Give the position of every malaria parasite and every leukocyte.
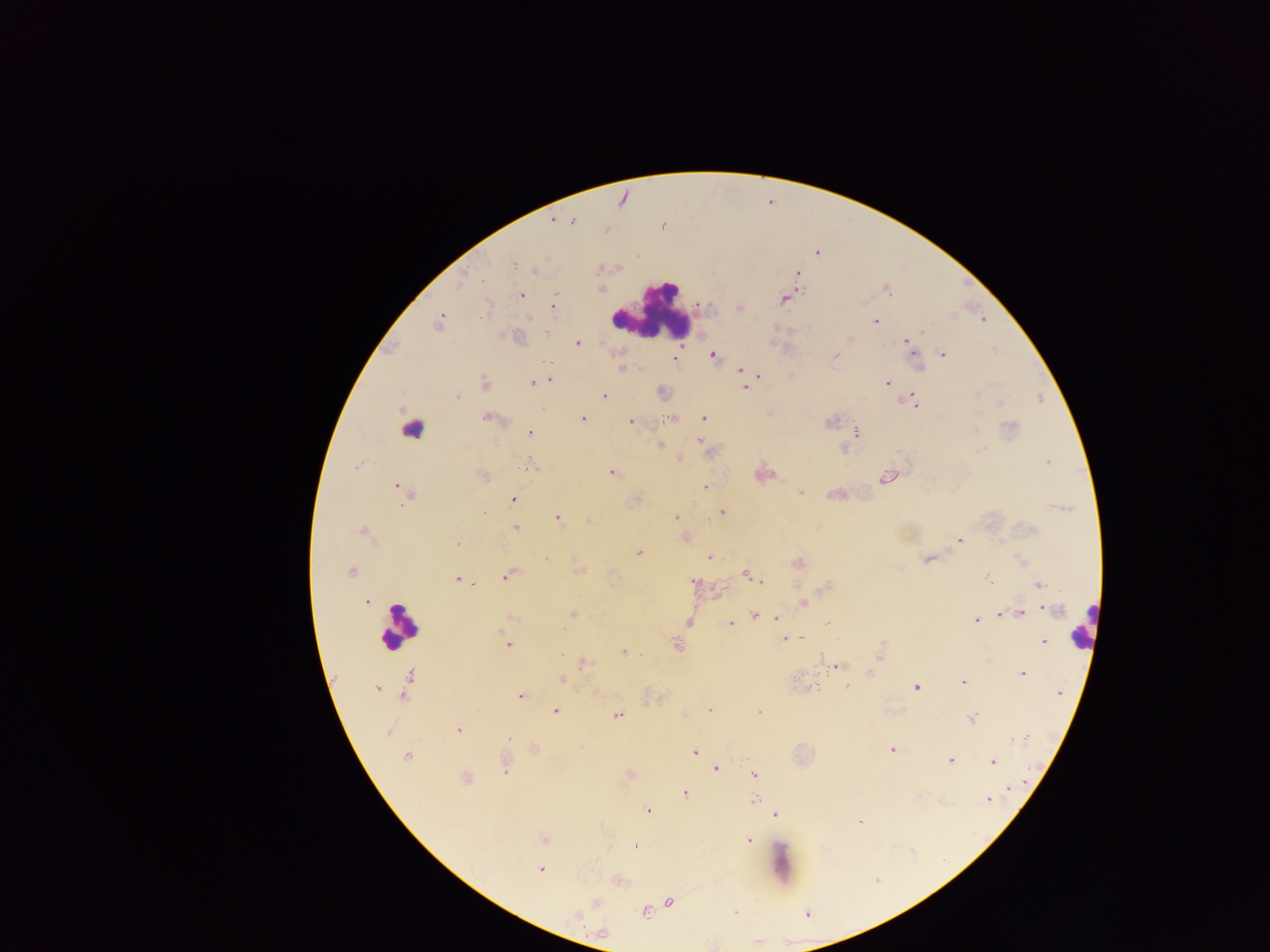

Approximate centers as (x, y) in pixels.
Malaria parasites: (553, 219), (562, 219), (572, 220), (816, 252), (638, 256), (534, 270), (797, 273), (460, 278), (600, 289), (886, 289), (519, 295), (784, 299), (552, 306), (740, 307), (486, 311), (439, 320), (875, 321), (982, 321), (546, 333), (852, 337), (576, 342), (906, 342), (913, 351), (941, 353), (712, 355), (835, 355), (674, 359), (917, 366), (623, 369), (741, 369), (757, 374), (549, 379), (534, 383), (887, 383), (484, 384), (745, 386), (661, 391), (977, 393), (604, 395), (905, 398), (911, 398), (999, 402), (915, 404), (487, 417), (582, 418), (669, 418), (703, 418), (829, 421), (630, 422), (855, 432), (529, 433), (699, 441), (660, 444), (843, 448), (679, 459), (1049, 461), (531, 466), (612, 472), (762, 473), (888, 475), (482, 476), (398, 486), (703, 486), (406, 492), (799, 492), (836, 494), (513, 500), (483, 512), (722, 512), (557, 518), (676, 518), (588, 520), (515, 528), (363, 531), (685, 537), (958, 539), (456, 543), (638, 552), (709, 557), (929, 558), (544, 559), (1021, 562), (797, 563), (580, 569), (351, 571), (508, 573), (746, 574), (987, 578), (458, 580), (760, 581), (693, 582), (1039, 584), (718, 592), (367, 602), (803, 603), (1042, 607), (1005, 613), (1020, 613), (572, 614), (755, 614), (763, 615), (1000, 615), (512, 617), (777, 619), (977, 620), (689, 621), (829, 622), (730, 623), (801, 638), (782, 639), (791, 639), (1043, 641), (507, 644), (677, 644), (623, 652), (879, 653), (582, 663), (835, 666), (869, 673), (1022, 673), (408, 678), (560, 678), (963, 682), (376, 687), (846, 687), (915, 687), (807, 688), (1059, 693), (520, 695), (710, 709), (555, 710), (758, 711), (684, 713), (617, 715), (972, 718), (457, 729), (388, 731), (509, 739), (1013, 742), (535, 748), (891, 749), (694, 752), (406, 757), (950, 759), (992, 761), (506, 764), (716, 768), (629, 774), (753, 775), (465, 779), (1008, 787), (685, 793), (754, 799), (988, 799), (940, 801), (648, 811), (774, 814), (860, 820), (542, 839), (748, 839), (635, 847), (541, 869), (616, 880), (596, 902), (669, 902), (644, 910), (575, 915), (602, 933).
Leukocytes: (653, 311), (411, 427), (400, 625), (1082, 627), (781, 863).

capture = mobile-phone photograph through a microscope
country = Ghana
field of view = single
preparation = thick blood film
image size = 1270×952 pixels